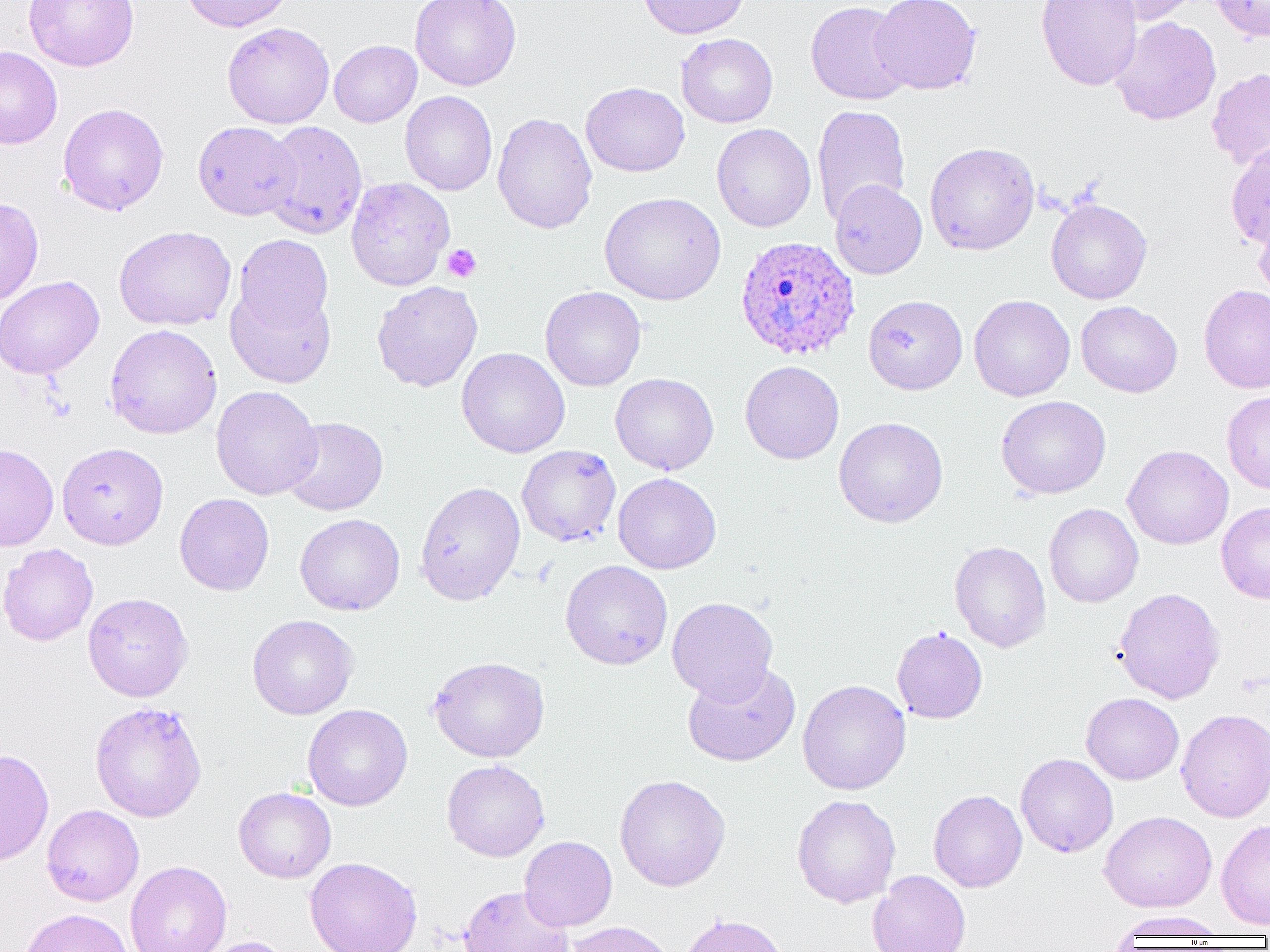
slide-level diagnosis = Plasmodium ovale
platelet locations = approximate bounding boxes as named x1/y1/x2/y2 corners in pixels: (x1=442, y1=244, x2=481, y2=283)
preparation = thin blood film
modality = light microscopy
image size = 1270×952 pixels
uninfected red blood cell locations = approximate bounding boxes as named x1/y1/x2/y2 corners in pixels: (x1=23, y1=0, x2=139, y2=72), (x1=180, y1=0, x2=293, y2=32), (x1=409, y1=0, x2=522, y2=91), (x1=636, y1=0, x2=749, y2=39), (x1=869, y1=0, x2=983, y2=95), (x1=1035, y1=0, x2=1143, y2=91), (x1=1099, y1=0, x2=1203, y2=25), (x1=1210, y1=0, x2=1270, y2=42), (x1=805, y1=1, x2=913, y2=105), (x1=1110, y1=17, x2=1222, y2=125), (x1=222, y1=22, x2=335, y2=129), (x1=676, y1=33, x2=778, y2=128), (x1=329, y1=40, x2=421, y2=127), (x1=0, y1=45, x2=62, y2=149), (x1=1207, y1=67, x2=1270, y2=171), (x1=580, y1=82, x2=689, y2=176), (x1=400, y1=91, x2=497, y2=196), (x1=58, y1=102, x2=169, y2=215), (x1=812, y1=104, x2=911, y2=224), (x1=492, y1=112, x2=598, y2=234), (x1=262, y1=120, x2=367, y2=238), (x1=193, y1=121, x2=300, y2=220), (x1=712, y1=123, x2=816, y2=232), (x1=924, y1=142, x2=1040, y2=256), (x1=1225, y1=142, x2=1270, y2=249), (x1=345, y1=177, x2=455, y2=291), (x1=829, y1=180, x2=927, y2=279), (x1=600, y1=192, x2=726, y2=305), (x1=0, y1=197, x2=44, y2=305), (x1=1045, y1=197, x2=1153, y2=305), (x1=1254, y1=208, x2=1270, y2=306), (x1=114, y1=225, x2=236, y2=331), (x1=233, y1=234, x2=334, y2=336), (x1=0, y1=275, x2=104, y2=379), (x1=372, y1=280, x2=483, y2=392), (x1=225, y1=284, x2=336, y2=388), (x1=1198, y1=284, x2=1270, y2=394), (x1=541, y1=286, x2=646, y2=391), (x1=864, y1=295, x2=968, y2=394), (x1=968, y1=295, x2=1075, y2=401), (x1=1076, y1=301, x2=1182, y2=398), (x1=104, y1=324, x2=222, y2=440), (x1=457, y1=347, x2=570, y2=457), (x1=740, y1=361, x2=844, y2=464), (x1=610, y1=373, x2=719, y2=475), (x1=211, y1=385, x2=322, y2=500), (x1=1222, y1=391, x2=1270, y2=494), (x1=996, y1=395, x2=1111, y2=499), (x1=281, y1=416, x2=388, y2=515), (x1=834, y1=417, x2=948, y2=528), (x1=57, y1=442, x2=169, y2=550), (x1=0, y1=443, x2=58, y2=552), (x1=517, y1=444, x2=621, y2=548), (x1=1122, y1=444, x2=1233, y2=549), (x1=613, y1=473, x2=721, y2=574), (x1=414, y1=481, x2=526, y2=605), (x1=174, y1=493, x2=274, y2=595), (x1=1216, y1=502, x2=1270, y2=604), (x1=1044, y1=503, x2=1143, y2=608), (x1=295, y1=513, x2=405, y2=616), (x1=949, y1=541, x2=1051, y2=652), (x1=0, y1=543, x2=98, y2=646), (x1=560, y1=560, x2=673, y2=670), (x1=1113, y1=587, x2=1226, y2=704), (x1=82, y1=593, x2=193, y2=701), (x1=666, y1=597, x2=778, y2=703), (x1=247, y1=614, x2=359, y2=720), (x1=892, y1=626, x2=988, y2=724), (x1=428, y1=655, x2=550, y2=762), (x1=682, y1=663, x2=801, y2=766), (x1=797, y1=679, x2=911, y2=795), (x1=1081, y1=692, x2=1184, y2=785), (x1=90, y1=701, x2=208, y2=822), (x1=302, y1=703, x2=413, y2=811), (x1=1175, y1=708, x2=1270, y2=822), (x1=0, y1=748, x2=54, y2=867), (x1=1016, y1=753, x2=1118, y2=858), (x1=442, y1=759, x2=550, y2=862), (x1=614, y1=774, x2=731, y2=891), (x1=233, y1=787, x2=336, y2=883), (x1=928, y1=789, x2=1027, y2=892), (x1=791, y1=794, x2=901, y2=908), (x1=41, y1=805, x2=144, y2=906), (x1=1099, y1=810, x2=1217, y2=913), (x1=1216, y1=818, x2=1270, y2=930), (x1=519, y1=836, x2=617, y2=931), (x1=305, y1=857, x2=423, y2=952), (x1=125, y1=860, x2=232, y2=952), (x1=868, y1=870, x2=971, y2=952), (x1=458, y1=885, x2=574, y2=952), (x1=19, y1=907, x2=133, y2=952), (x1=1109, y1=911, x2=1231, y2=939), (x1=678, y1=913, x2=790, y2=952), (x1=563, y1=921, x2=677, y2=952), (x1=198, y1=936, x2=295, y2=952)
Plasmodium ovale-infected red blood cell locations = approximate bounding boxes as named x1/y1/x2/y2 corners in pixels: (x1=734, y1=235, x2=860, y2=360)
field of view = one of a larger specimen
magnification = 1000x